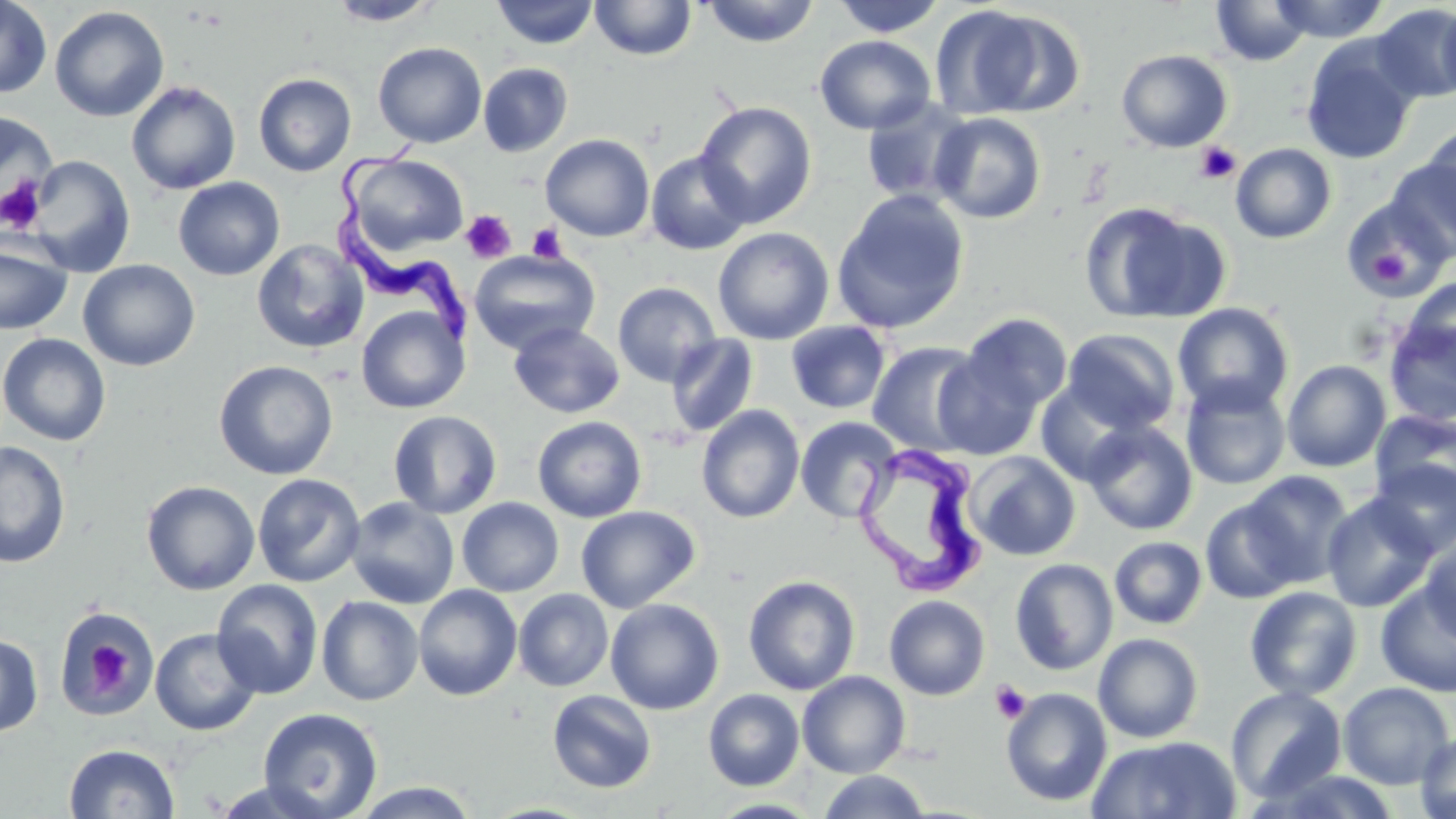

{
  "trypanosoma_brucei_locations": "approximate bounding boxes as (x1,y1)-(x2,y2) corner pairs in pixels: (335,135)-(484,338), (853,442)-(991,600)",
  "slide_level_diagnosis": "Trypanosoma brucei",
  "magnification": "1000x",
  "modality": "optical microscopy",
  "platelet_locations": "approximate bounding boxes as (x1,y1)-(x2,y2) corner pairs in pixels: (1195,141)-(1241,185), (0,177)-(50,234), (461,210)-(516,264), (527,223)-(567,263), (1366,249)-(1415,289), (79,633)-(136,695), (990,680)-(1032,725)",
  "uninfected_red_blood_cell_locations": "approximate bounding boxes as (x1,y1)-(x2,y2) corner pairs in pixels: (0,0)-(52,98), (325,0)-(442,26), (491,0)-(599,49), (701,0)-(821,47), (831,0)-(947,37), (1270,0)-(1388,42), (590,1)-(697,60), (1211,1)-(1312,67), (1436,1)-(1456,104), (1370,3)-(1456,104), (929,5)-(1044,119), (49,6)-(169,121), (978,9)-(1088,118), (814,35)-(936,135), (1300,36)-(1420,164), (373,42)-(487,148), (1116,49)-(1233,152), (478,62)-(573,157), (253,73)-(356,177), (126,81)-(241,195), (860,96)-(977,207), (694,101)-(818,228), (0,111)-(60,222), (929,112)-(1046,224), (1422,122)-(1456,230), (540,134)-(655,241), (1230,143)-(1337,243), (645,150)-(753,255), (344,154)-(469,255), (27,155)-(136,277), (1386,159)-(1456,263), (173,177)-(285,280), (832,189)-(971,334), (1340,195)-(1451,300), (1079,201)-(1230,325), (713,227)-(834,344), (0,236)-(73,335), (251,239)-(370,354), (469,248)-(600,356), (78,259)-(200,371), (1400,277)-(1456,377), (612,282)-(721,387), (1172,302)-(1294,416), (356,305)-(469,414), (961,312)-(1073,413), (1383,315)-(1456,426), (786,321)-(892,414), (508,322)-(625,418), (1062,329)-(1181,435), (0,333)-(111,446), (666,334)-(758,438), (868,341)-(986,457), (933,352)-(1041,460), (213,360)-(338,480), (1282,360)-(1392,472), (1180,378)-(1291,490), (1035,380)-(1143,487), (696,405)-(805,524), (388,410)-(502,519), (1370,410)-(1456,509), (532,416)-(647,523), (795,416)-(902,525), (1082,421)-(1198,535), (0,440)-(72,568), (965,450)-(1081,561), (1369,459)-(1456,559), (1240,470)-(1355,588), (252,473)-(366,587), (141,480)-(260,595), (1321,492)-(1439,613), (346,497)-(460,609), (457,497)-(564,597), (1201,497)-(1303,603), (576,505)-(700,613), (1109,536)-(1208,629), (1419,536)-(1455,647), (1009,558)-(1118,676), (743,575)-(861,695), (211,579)-(324,699), (1375,581)-(1456,698), (413,584)-(523,701), (1244,586)-(1363,701), (513,589)-(614,692), (316,595)-(424,706), (884,595)-(990,700), (605,598)-(725,715), (53,610)-(161,718), (149,627)-(262,736), (0,633)-(43,738), (1092,633)-(1204,743), (797,671)-(911,778), (1337,681)-(1455,789), (1225,685)-(1347,804), (1000,687)-(1113,807), (547,689)-(657,793), (703,689)-(805,791), (257,707)-(383,819), (1415,730)-(1456,819), (1086,735)-(1242,818), (64,743)-(179,818), (1255,767)-(1407,819), (818,770)-(932,818), (206,778)-(338,818), (351,781)-(481,818), (706,798)-(825,819)",
  "stain": "May-Grünwald-Giemsa",
  "field_of_view": "one of a larger specimen",
  "image_size": "1456×819 pixels",
  "preparation": "thin blood smear"
}